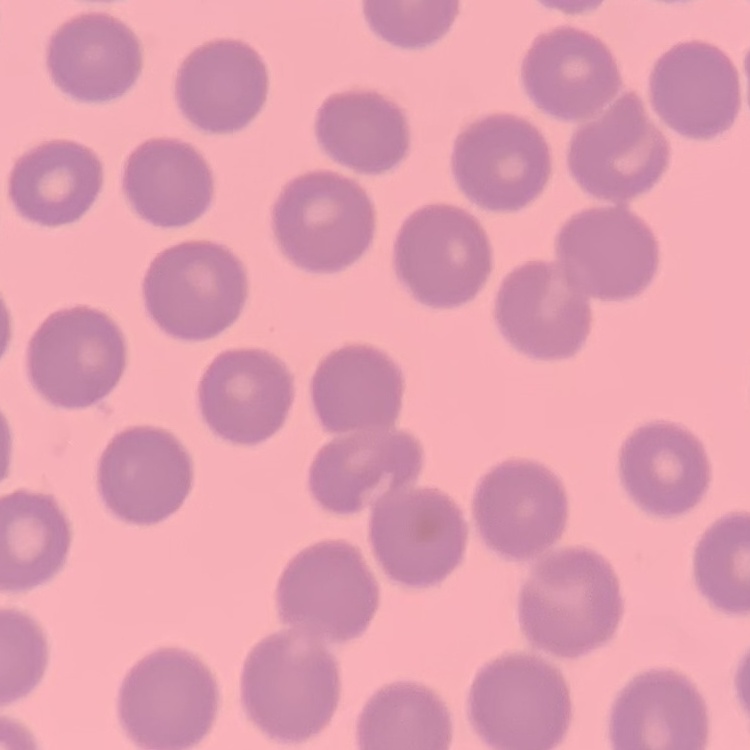

The erythrocytes exhibit no rouleaux formation. Thin blood smear. Stained with either Field's or Giemsa. Square crop of a larger photomicrograph.